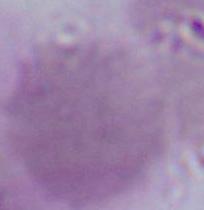

1000x magnification. A red blood cell is shown. Micrograph.